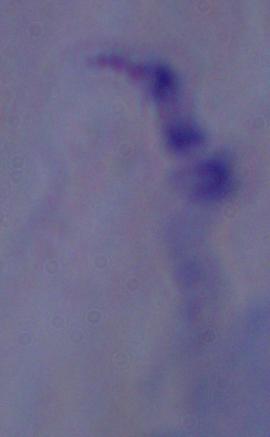
1000x magnification. A trypanosome is shown. Photomicrograph.